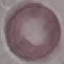

Summary:
  - Result: negative for malaria parasites
  - Image type: automatically extracted cell patch, resized to 64 × 64 pixels
  - Preparation: thin smear
  - Capture: smartphone through the microscope eyepiece
  - Stain: Giemsa